Locate every leukocyte (white blood cell).
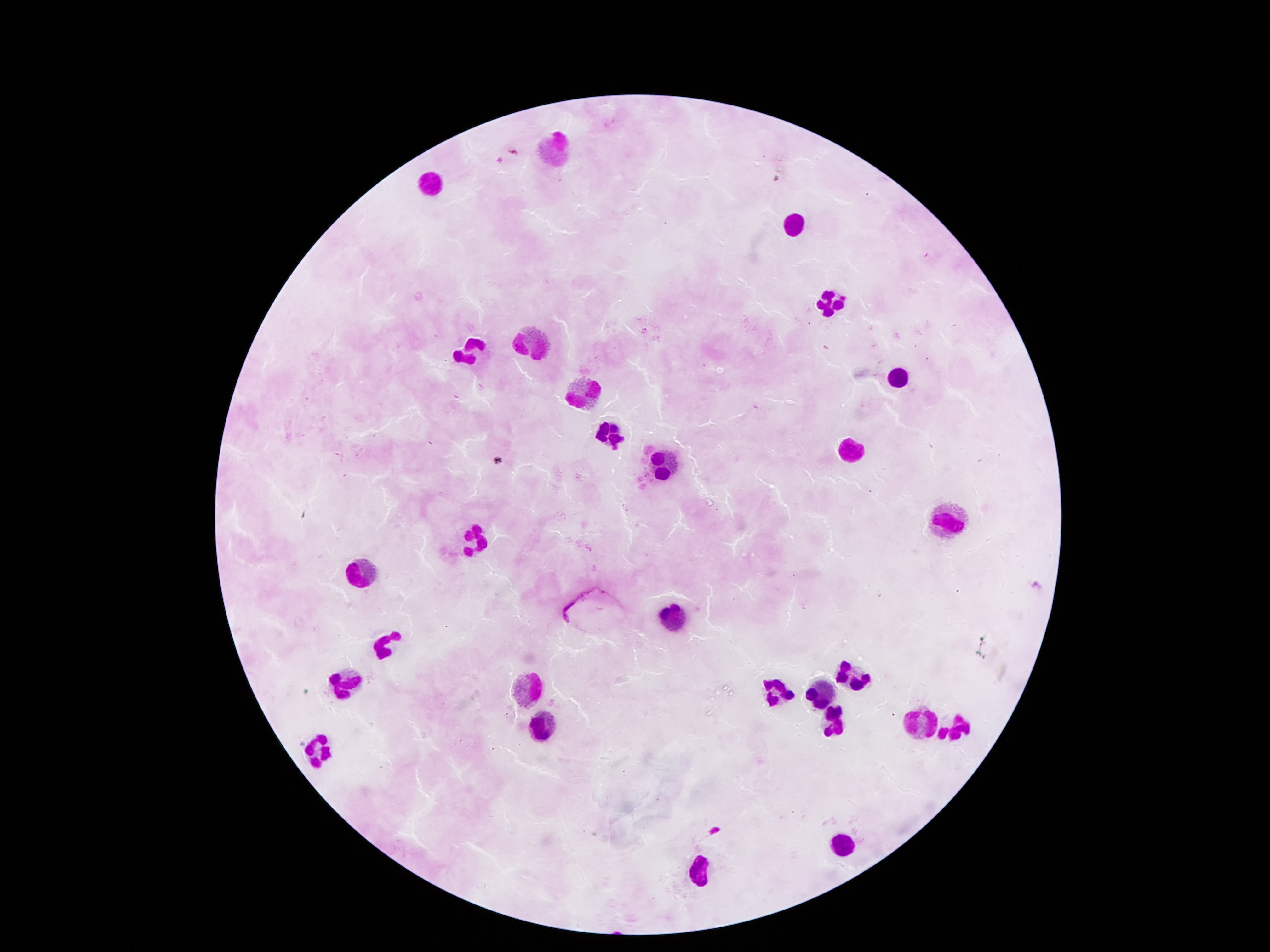
Approximate centers as {x, y} in pixels.
Leukocytes: {556, 148}, {436, 185}, {794, 224}, {823, 301}, {532, 343}, {472, 349}, {901, 380}, {579, 395}, {608, 430}, {849, 449}, {664, 461}, {942, 515}, {469, 542}, {355, 575}, {672, 616}, {391, 642}, {849, 673}, {349, 678}, {528, 686}, {819, 687}, {779, 689}, {827, 721}, {921, 723}, {954, 725}, {542, 728}, {317, 751}, {840, 846}, {697, 872}.

Summary:
  - Image size: 1270×952 pixels
  - Field of view: one from this slide
  - Preparation: thick blood smear
  - Magnification: 100x
  - Capture: smartphone camera through the microscope eyepiece
  - Stain: Giemsa
  - Patient malaria status: not infected